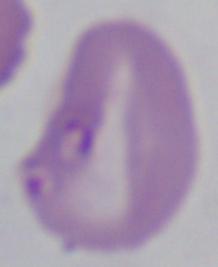
magnification = 1000x
identification = Babesia
modality = micrograph